Identify the cell.
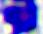
A leukocyte.

modality = micrograph
magnification = 400x